Name the parasite shown.
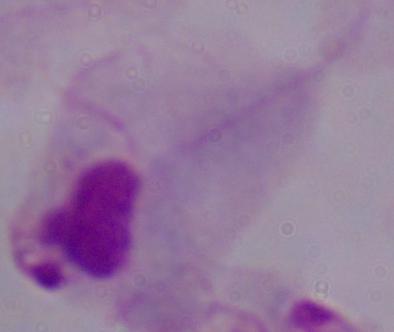
This is a trichomonad.

modality = micrograph
magnification = 1000x